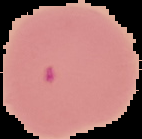

From a thin blood film. Cell region segmented out of the field of view; the surrounding area is masked to black. Malaria status: parasitized. Image is 142×139 pixels.